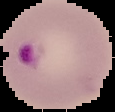
Summary:
  - Result: Plasmodium parasites detected
  - Image type: segmented cell region with the area outside set to black
  - Preparation: thin blood smear
  - Image size: 115×112 pixels